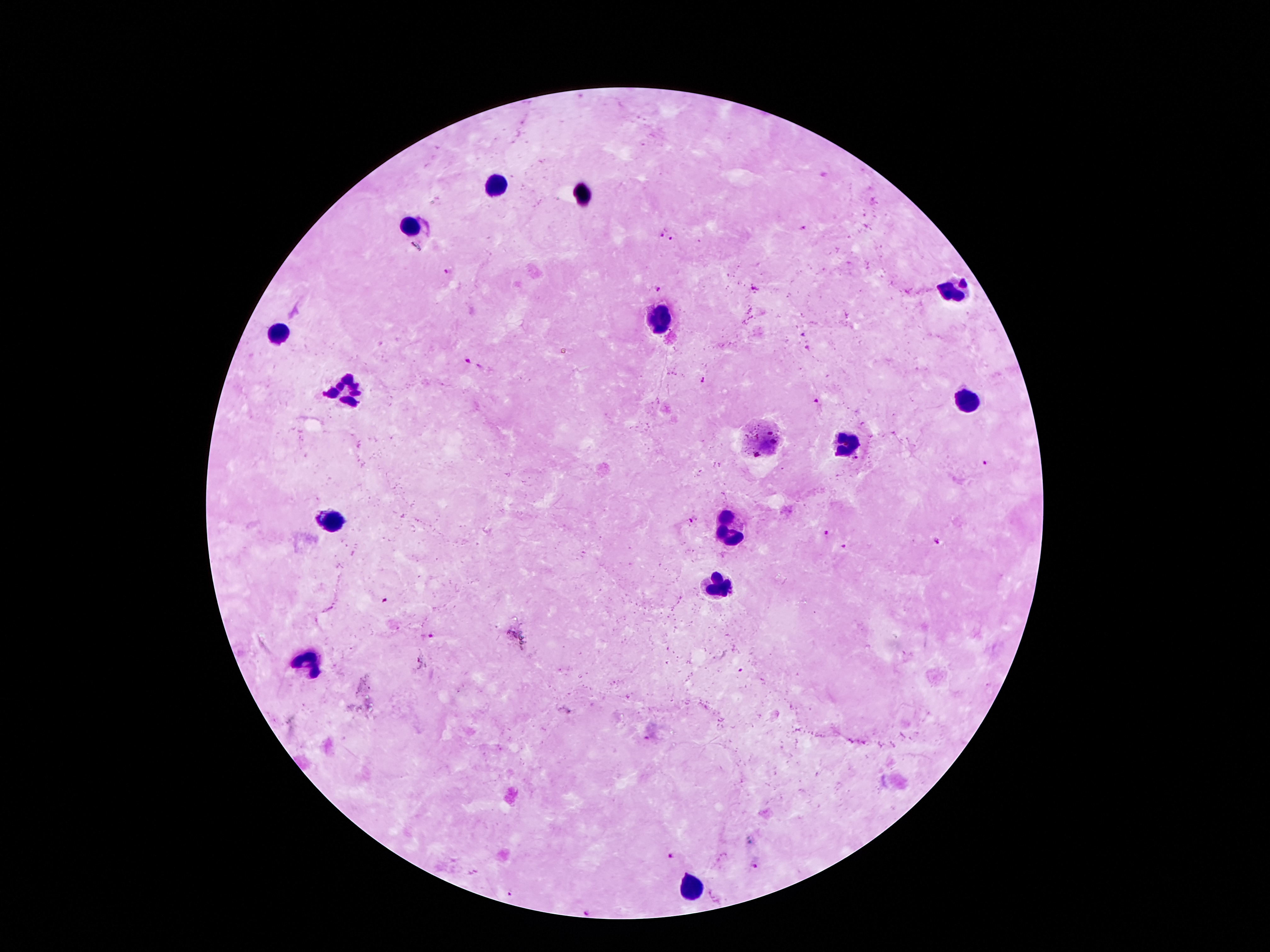

image_size: 1270×952 pixels
malaria_parasite_locations: 'approximate centers as {x, y} in pixels: {802, 228}, {662, 233}, {672, 239}, {446, 272}, {660, 289}, {753, 289}, {803, 335}, {808, 348}, {470, 361}, {702, 380}, {816, 401}, {984, 464}, {691, 520}, {827, 533}, {936, 539}, {844, 545}, {431, 636}, {646, 737}, {671, 855}, {755, 867}, {509, 894}, {589, 912}'
stain: Giemsa
capture: smartphone camera through the microscope eyepiece
preparation: thick peripheral-blood smear
field_of_view: one from this slide
patient_malaria_status: infected with Plasmodium falciparum
leukocyte_locations: 'approximate centers as {x, y} in pixels: {500, 185}, {411, 229}, {953, 292}, {661, 317}, {279, 337}, {346, 390}, {967, 401}, {844, 447}, {335, 521}, {729, 533}, {724, 589}, {309, 656}, {689, 889}'
magnification: 100x